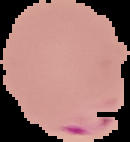

image type = cell region segmented out of the field of view; surrounding area masked to black
preparation = thin blood smear
image size = 130×142 pixels
malaria status = parasitized